Report the malaria status of this cell.
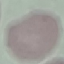

Uninfected.

Summary:
  - Image type: cell patch, automatically extracted from a larger field of view and resized to 64 × 64 pixels
  - Stain: Giemsa
  - Capture: smartphone camera at the microscope eyepiece
  - Preparation: thin smear